Give the position of every Plasmodium parasite.
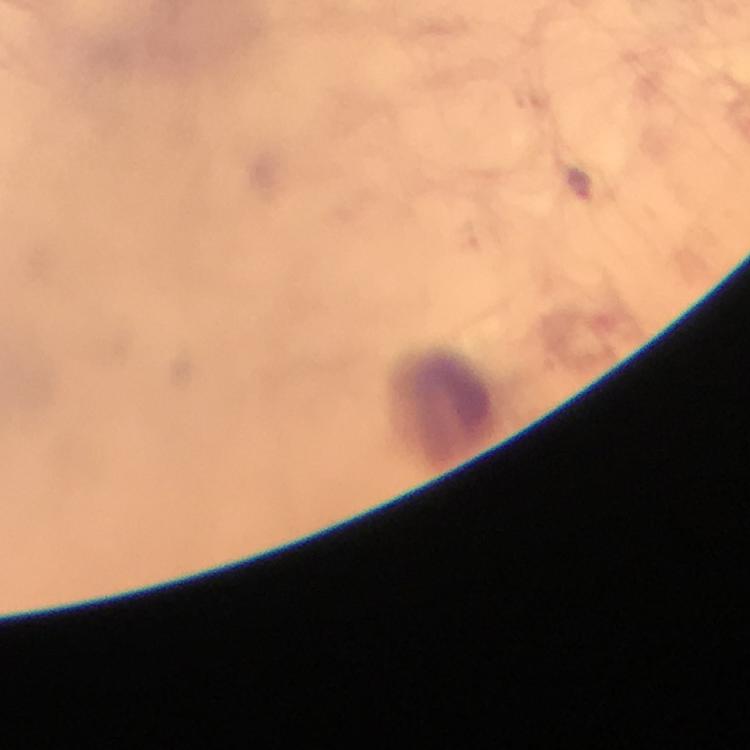

Approximate centers as [x, y] in pixels.
Plasmodium parasites: [583, 190].

capture = smartphone photograph through a microscope
immersion oil = used
preparation = thick blood film
context = from a malaria diagnostic workup
magnification = 100x
stain = Giemsa
cropped from = a single field of view
image size = 750×750 pixels